Assess this cell for malaria.
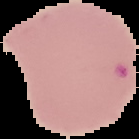
Parasitized.

From a thin blood smear. The area outside the segmented cell region is set to black. Image is 139×139 pixels.